Name the blood parasite species.
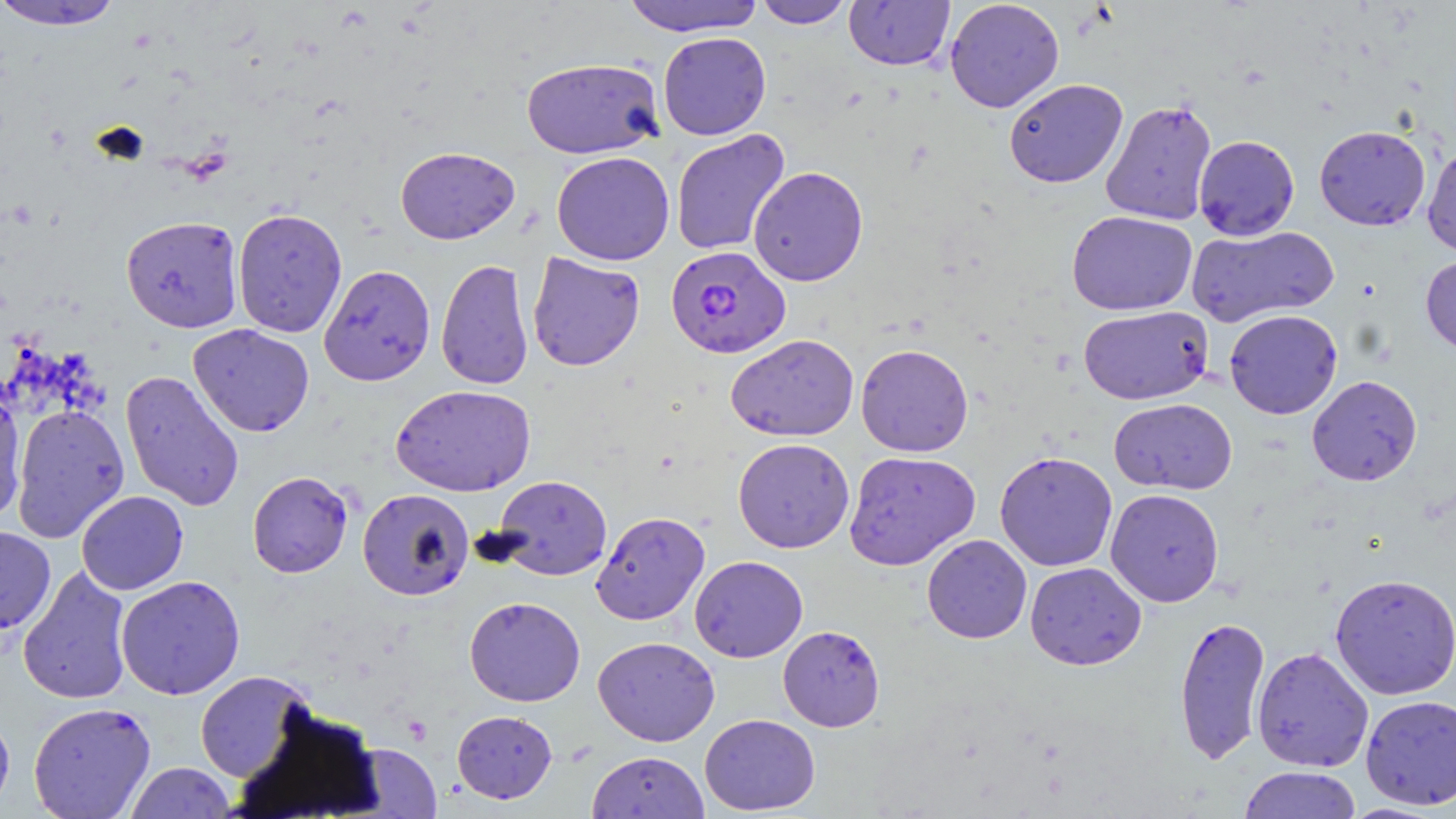
Plasmodium falciparum.

Summary:
  - Coordinate format: approximate bounding boxes as named x1/y1/x2/y2 corners in pixels
  - Uninfected red blood cell locations: (x1=1, y1=0, x2=126, y2=31), (x1=622, y1=0, x2=765, y2=37), (x1=754, y1=0, x2=853, y2=28), (x1=844, y1=0, x2=955, y2=70), (x1=945, y1=0, x2=1064, y2=113), (x1=658, y1=31, x2=771, y2=140), (x1=521, y1=57, x2=664, y2=160), (x1=1004, y1=78, x2=1128, y2=188), (x1=1100, y1=98, x2=1217, y2=226), (x1=1314, y1=125, x2=1431, y2=230), (x1=670, y1=129, x2=790, y2=257), (x1=1193, y1=135, x2=1299, y2=240), (x1=1422, y1=142, x2=1456, y2=257), (x1=395, y1=146, x2=520, y2=245), (x1=551, y1=151, x2=675, y2=266), (x1=748, y1=166, x2=869, y2=286), (x1=232, y1=208, x2=347, y2=338), (x1=1067, y1=210, x2=1197, y2=316), (x1=121, y1=215, x2=243, y2=332), (x1=1187, y1=225, x2=1338, y2=327), (x1=527, y1=252, x2=645, y2=371), (x1=1420, y1=255, x2=1456, y2=356), (x1=436, y1=258, x2=534, y2=390), (x1=319, y1=264, x2=435, y2=386), (x1=1077, y1=305, x2=1213, y2=405), (x1=1224, y1=309, x2=1343, y2=419), (x1=188, y1=323, x2=315, y2=437), (x1=726, y1=333, x2=859, y2=441), (x1=855, y1=343, x2=974, y2=457), (x1=120, y1=370, x2=244, y2=512), (x1=1306, y1=375, x2=1422, y2=486), (x1=391, y1=384, x2=536, y2=497), (x1=0, y1=388, x2=28, y2=524), (x1=1109, y1=397, x2=1237, y2=494), (x1=10, y1=404, x2=129, y2=542), (x1=732, y1=438, x2=855, y2=553), (x1=843, y1=450, x2=981, y2=570), (x1=994, y1=450, x2=1118, y2=571), (x1=247, y1=470, x2=354, y2=578), (x1=493, y1=475, x2=612, y2=580), (x1=357, y1=488, x2=474, y2=601), (x1=1105, y1=488, x2=1224, y2=607), (x1=76, y1=490, x2=189, y2=595), (x1=591, y1=511, x2=710, y2=625), (x1=0, y1=526, x2=56, y2=633), (x1=921, y1=534, x2=1032, y2=644), (x1=689, y1=555, x2=808, y2=662), (x1=1024, y1=562, x2=1146, y2=670), (x1=18, y1=566, x2=134, y2=705), (x1=1329, y1=573, x2=1456, y2=700), (x1=115, y1=575, x2=246, y2=700), (x1=464, y1=596, x2=586, y2=707), (x1=1174, y1=614, x2=1270, y2=765), (x1=778, y1=625, x2=885, y2=731), (x1=593, y1=636, x2=720, y2=746), (x1=1251, y1=646, x2=1374, y2=772), (x1=195, y1=670, x2=315, y2=783), (x1=1360, y1=695, x2=1456, y2=810), (x1=28, y1=701, x2=156, y2=818), (x1=0, y1=709, x2=14, y2=814), (x1=452, y1=710, x2=557, y2=804), (x1=700, y1=713, x2=820, y2=815), (x1=351, y1=744, x2=442, y2=817), (x1=587, y1=751, x2=710, y2=819), (x1=125, y1=762, x2=237, y2=819), (x1=1238, y1=766, x2=1361, y2=819)
  - Plasmodium falciparum-infected red blood cell locations: (x1=665, y1=246, x2=791, y2=358)
  - Modality: optical microscopy
  - Stain: May-Grünwald-Giemsa
  - Image size: 1456×819 pixels
  - Preparation: thin blood film
  - Magnification: 1000x
  - Field of view: single